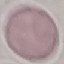

Result: negative for malaria parasites. Cell patch, automatically extracted from a larger field of view and resized to 64 × 64 pixels. Thin blood smear. Giemsa-stained preparation. Acquired by smartphone through the microscope eyepiece.